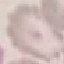
Malaria status: uninfected. Automatically extracted cell patch, resized to 64 × 64 pixels. Thin blood smear. Giemsa-stained preparation. Photographed with a smartphone camera at the microscope eyepiece.